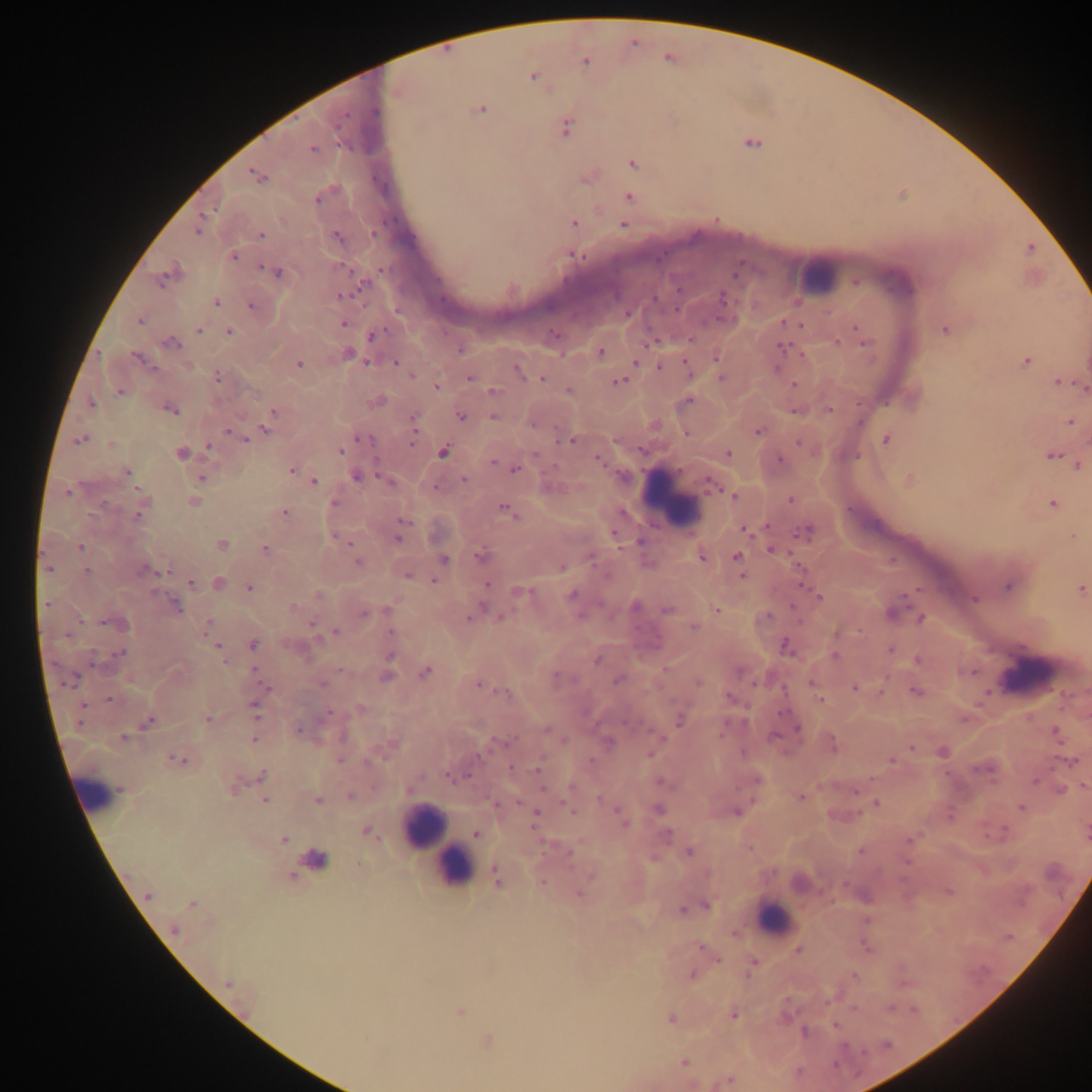
Approximate centers as {x, y} in pixels.
Summary:
  - Plasmodium parasite locations: {585, 62}, {533, 76}, {480, 110}, {374, 112}, {347, 114}, {566, 126}, {312, 149}, {318, 202}, {576, 223}, {623, 225}, {196, 231}, {261, 235}, {234, 256}, {579, 256}, {342, 266}, {262, 267}, {380, 269}, {276, 270}, {161, 281}, {853, 281}, {361, 287}, {675, 289}, {338, 295}, {443, 297}, {721, 297}, {216, 303}, {251, 304}, {676, 309}, {626, 312}, {140, 322}, {782, 322}, {344, 324}, {801, 324}, {854, 326}, {198, 331}, {382, 331}, {227, 332}, {691, 337}, {371, 338}, {657, 340}, {836, 340}, {171, 342}, {864, 345}, {782, 346}, {601, 350}, {800, 354}, {135, 355}, {716, 356}, {365, 361}, {685, 361}, {1027, 361}, {635, 362}, {297, 363}, {397, 363}, {659, 366}, {515, 367}, {777, 367}, {412, 376}, {721, 377}, {217, 378}, {469, 378}, {542, 378}, {619, 380}, {1057, 381}, {795, 385}, {436, 387}, {1083, 388}, {492, 391}, {569, 391}, {118, 392}, {689, 400}, {91, 403}, {858, 405}, {828, 409}, {172, 411}, {794, 411}, {273, 412}, {459, 417}, {412, 418}, {493, 418}, {1070, 421}, {265, 429}, {259, 430}, {757, 431}, {229, 432}, {413, 433}, {358, 438}, {80, 440}, {246, 440}, {559, 440}, {571, 440}, {884, 440}, {1085, 441}, {797, 442}, {412, 444}, {208, 447}, {642, 451}, {341, 452}, {443, 452}, {180, 454}, {535, 454}, {727, 454}, {1055, 454}, {857, 455}, {1049, 455}, {377, 458}, {597, 459}, {494, 460}, {781, 460}, {1077, 465}, {515, 469}, {127, 471}, {291, 471}, {356, 475}, {379, 476}, {200, 478}, {909, 479}, {463, 480}, {314, 481}, {709, 483}, {137, 488}, {434, 488}, {733, 496}, {788, 500}, {334, 501}, {1052, 502}, {503, 509}, {282, 512}, {622, 512}, {138, 514}, {401, 521}, {765, 525}, {744, 529}, {800, 532}, {748, 533}, {615, 538}, {399, 539}, {348, 541}, {639, 542}, {222, 544}, {80, 547}, {265, 549}, {769, 549}, {477, 556}, {736, 556}, {445, 558}, {357, 563}, {797, 567}, {47, 569}, {86, 569}, {563, 569}, {50, 570}, {146, 570}, {168, 570}, {407, 575}, {742, 575}, {432, 580}, {191, 582}, {487, 583}, {249, 590}, {918, 590}, {531, 592}, {517, 593}, {573, 594}, {818, 597}, {973, 597}, {903, 598}, {45, 605}, {483, 606}, {295, 607}, {793, 607}, {386, 610}, {667, 610}, {369, 611}, {716, 611}, {363, 612}, {471, 613}, {767, 616}, {500, 617}, {916, 617}, {921, 617}, {468, 619}, {311, 622}, {104, 623}, {207, 625}, {693, 626}, {391, 631}, {859, 631}, {336, 632}, {318, 638}, {786, 642}, {253, 645}, {217, 646}, {890, 650}, {123, 652}, {118, 654}, {834, 656}, {390, 657}, {597, 661}, {916, 661}, {225, 662}, {254, 669}, {341, 671}, {974, 671}, {425, 672}, {555, 675}, {384, 677}, {616, 680}, {70, 683}, {697, 683}, {65, 684}, {322, 684}, {753, 684}, {810, 684}, {478, 686}, {269, 688}, {854, 688}, {784, 691}, {915, 691}, {880, 692}, {499, 694}, {507, 694}, {727, 696}, {110, 700}, {821, 700}, {83, 706}, {254, 707}, {978, 707}, {330, 712}, {783, 713}, {257, 715}, {209, 719}, {625, 720}, {680, 720}, {80, 723}, {147, 723}, {298, 729}, {796, 729}, {1053, 729}, {548, 730}, {720, 732}, {773, 736}, {124, 737}, {253, 740}, {508, 740}, {563, 741}, {490, 747}, {910, 747}, {743, 752}, {649, 755}, {479, 756}, {172, 758}, {185, 759}, {338, 760}, {367, 761}, {589, 761}, {891, 761}, {1071, 762}, {510, 767}, {536, 768}, {262, 774}, {468, 774}, {946, 774}, {422, 776}, {447, 777}, {871, 778}, {660, 781}, {1034, 782}, {1083, 785}, {570, 786}, {233, 787}, {541, 788}, {410, 789}, {1058, 789}, {854, 790}, {349, 796}, {598, 796}, {800, 797}, {753, 799}, {264, 800}, {318, 800}, {876, 801}, {517, 803}, {562, 803}, {1021, 808}, {617, 810}, {572, 812}, {736, 812}, {535, 813}, {860, 815}, {949, 815}, {625, 825}, {1004, 829}, {365, 830}, {475, 834}, {668, 835}, {985, 835}, {282, 839}, {908, 840}, {748, 849}, {861, 851}, {689, 852}, {569, 855}, {653, 857}, {359, 863}, {590, 875}, {542, 883}, {844, 883}, {948, 892}, {578, 894}, {148, 897}, {191, 905}, {706, 905}, {681, 909}, {173, 931}, {732, 933}, {1005, 939}, {1008, 939}, {699, 946}, {866, 947}, {798, 949}, {717, 960}, {754, 961}, {691, 973}, {747, 976}, {854, 976}, {226, 984}, {903, 984}, {785, 999}, {853, 1007}, {890, 1007}, {912, 1009}, {459, 1012}, {732, 1015}, {671, 1019}, {836, 1026}, {804, 1031}, {885, 1045}, {864, 1051}, {685, 1061}, {798, 1071}, {730, 1079}
  - Leukocyte locations: {668, 502}, {1023, 675}, {105, 803}, {449, 850}, {781, 919}
  - Preparation: thick blood film
  - Field of view: single
  - Image size: 1092×1092 pixels
  - Country: Ghana
  - Capture: mobile-phone photograph through a microscope